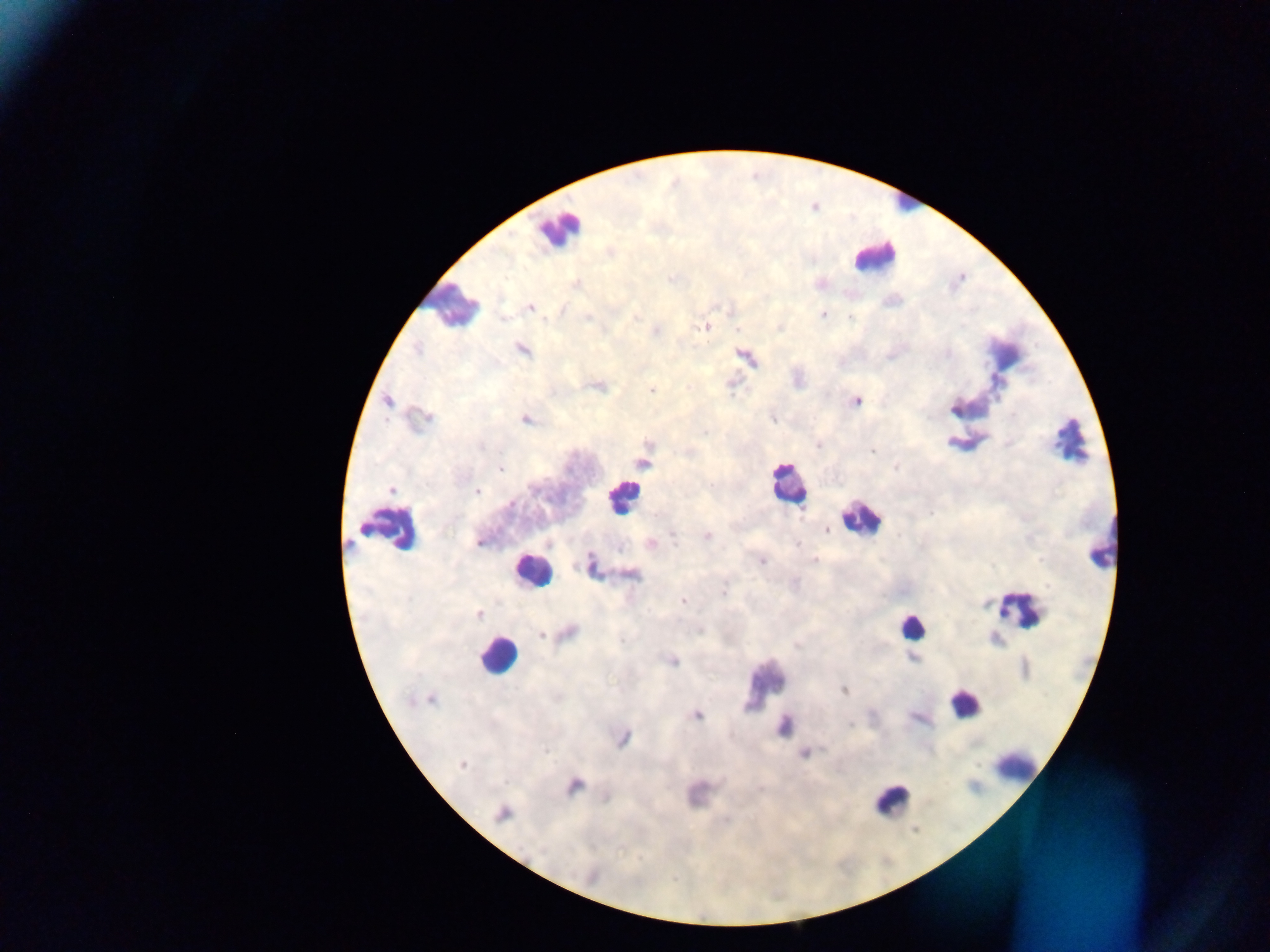

image size = 1270×952 pixels
preparation = thick blood smear
malaria parasite locations = approximate centers as {x, y} in pixels: {576, 283}, {531, 307}, {823, 315}, {636, 316}, {850, 317}, {588, 318}, {503, 319}, {704, 327}, {656, 331}, {417, 350}, {523, 350}, {948, 353}, {597, 386}, {688, 387}, {652, 389}, {388, 401}, {855, 402}, {953, 408}, {422, 419}, {525, 419}, {772, 419}, {705, 432}, {648, 443}, {819, 445}, {480, 447}, {872, 451}, {643, 463}, {896, 467}, {500, 468}, {711, 485}, {391, 490}, {477, 491}, {932, 513}, {363, 529}, {827, 530}, {673, 536}, {707, 536}, {479, 543}, {798, 543}, {651, 544}, {815, 560}, {762, 561}, {591, 564}, {631, 575}, {724, 592}, {682, 600}, {478, 614}, {568, 633}, {542, 634}, {621, 640}, {797, 646}, {672, 660}, {844, 690}, {431, 699}, {697, 716}, {850, 724}, {783, 726}, {623, 738}, {545, 751}, {804, 753}, {462, 764}, {574, 785}, {606, 798}, {502, 814}, {726, 820}, {591, 876}
leukocyte locations = approximate centers as {x, y} in pixels: {906, 205}, {557, 228}, {874, 256}, {452, 303}, {1070, 441}, {788, 485}, {622, 497}, {861, 519}, {394, 528}, {1104, 542}, {530, 571}, {1020, 609}, {911, 626}, {496, 656}, {765, 681}, {964, 703}, {1015, 765}, {892, 800}
capture = mobile-phone photograph through a microscope
field of view = single
country = Ghana